Give the extent of all Plasmodium vivax-infected red blood cells.
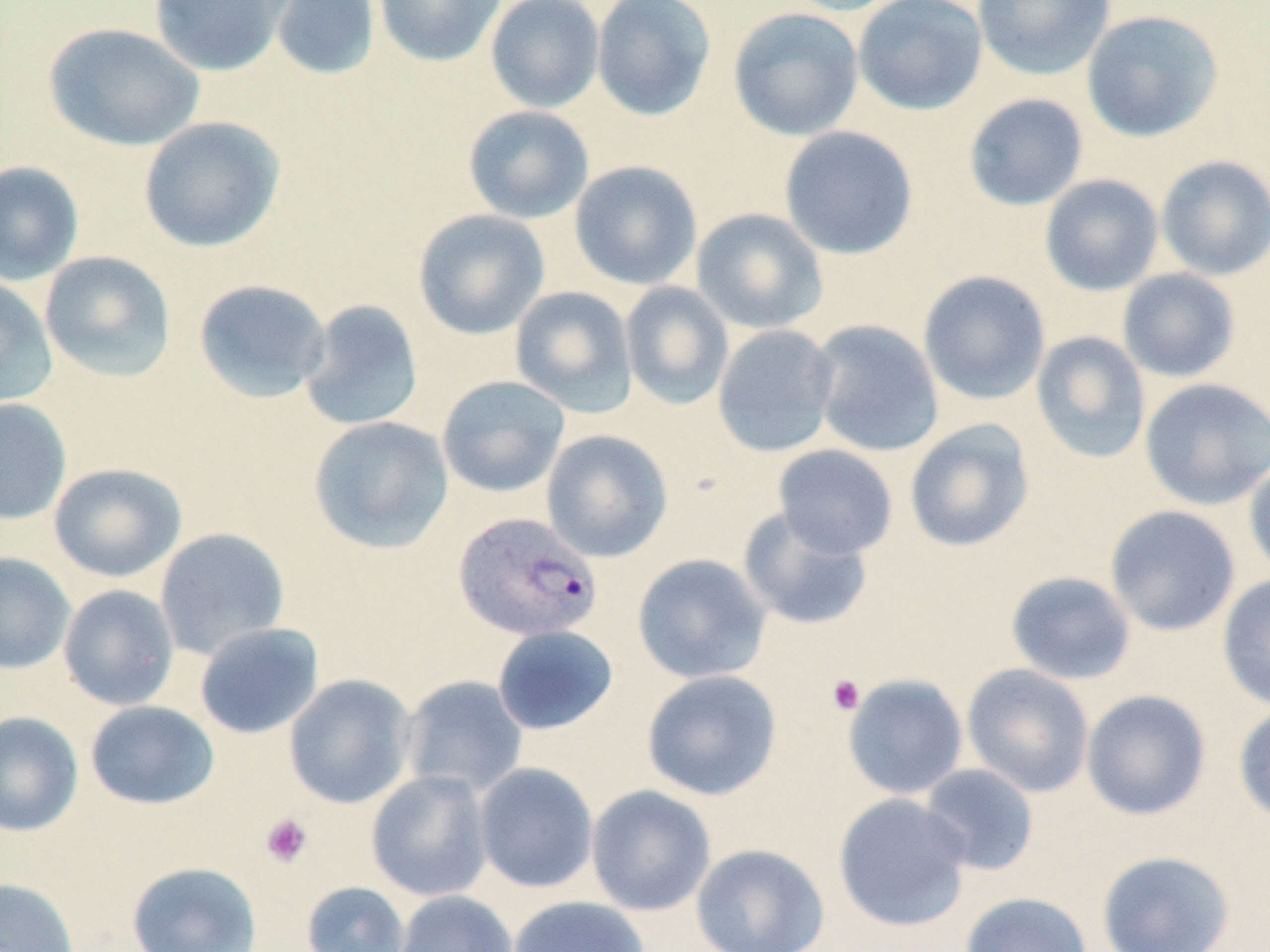

Approximate bounding boxes as (x1,y1)-(x2,y2) corner pairs in pixels.
Plasmodium vivax-infected red blood cells: (454,511)-(604,643).

{
  "slide_level_diagnosis": "Plasmodium vivax",
  "uninfected_red_blood_cell_locations": "approximate bounding boxes as (x1,y1)-(x2,y2) corner pairs in pixels: (148,0)-(288,77), (269,0)-(381,81), (373,0)-(506,68), (485,0)-(605,113), (592,0)-(717,122), (780,0)-(912,16), (853,0)-(988,116), (972,0)-(1116,81), (728,7)-(864,141), (1081,10)-(1224,143), (43,22)-(205,152), (963,93)-(1089,211), (462,105)-(595,224), (138,116)-(286,253), (779,126)-(919,260), (1156,155)-(1270,281), (0,161)-(85,286), (569,161)-(702,290), (1040,175)-(1164,296), (691,208)-(828,335), (413,209)-(550,340), (39,251)-(177,384), (1118,268)-(1241,383), (918,270)-(1051,405), (0,276)-(59,410), (192,278)-(332,404), (619,281)-(735,410), (509,286)-(638,418), (298,299)-(424,432), (807,319)-(944,458), (712,324)-(840,457), (1031,331)-(1151,465), (437,375)-(569,498), (1139,377)-(1270,510), (0,397)-(72,525), (308,415)-(454,554), (903,419)-(1035,553), (541,429)-(673,562), (772,444)-(898,559), (1244,457)-(1270,581), (48,462)-(186,583), (737,505)-(873,631), (1105,505)-(1240,637), (154,527)-(290,660), (0,552)-(76,675), (632,553)-(772,684), (1005,570)-(1136,685), (1217,573)-(1270,711), (58,584)-(179,710), (194,622)-(324,739), (491,625)-(619,736), (961,663)-(1095,798), (641,669)-(783,801), (284,674)-(417,809), (843,674)-(968,800), (400,675)-(528,799), (1081,689)-(1212,820), (84,700)-(220,811), (1233,702)-(1270,825), (0,711)-(84,837), (473,762)-(599,894), (919,763)-(1040,877), (365,770)-(494,902), (586,785)-(716,916), (833,793)-(972,932), (690,843)-(830,952), (1096,850)-(1235,952), (126,861)-(262,952), (0,878)-(81,952), (301,881)-(411,952), (394,890)-(518,952), (959,891)-(1093,952), (508,895)-(650,952)",
  "platelet_locations": "approximate bounding boxes as (x1,y1)-(x2,y2) corner pairs in pixels: (827,674)-(866,715), (259,813)-(313,868)",
  "image_size": "1270×952 pixels",
  "field_of_view": "single",
  "preparation": "thin blood film",
  "modality": "optical microscopy",
  "stain": "May-Grünwald-Giemsa",
  "magnification": "1000x"
}